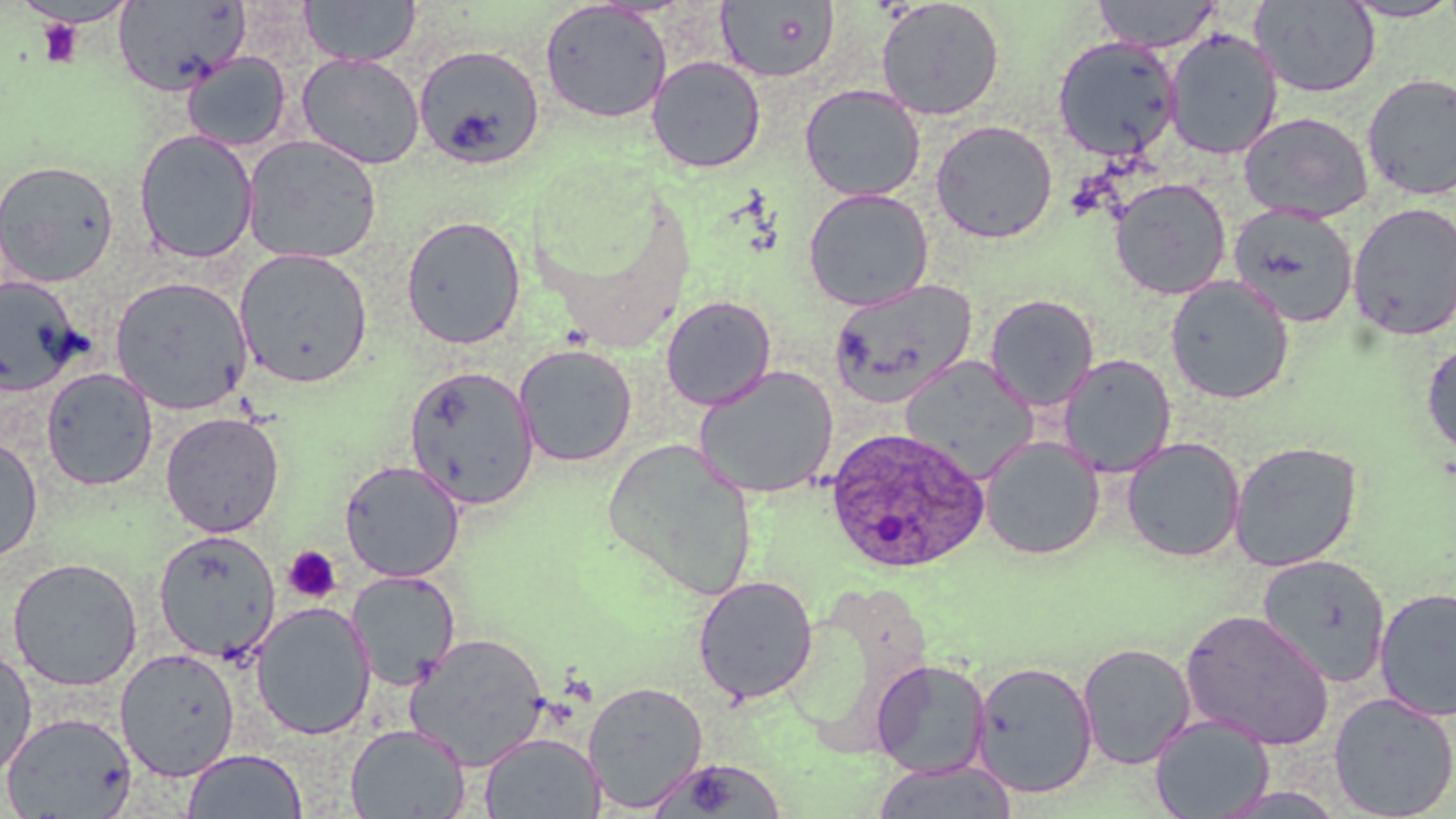

slide-level diagnosis = Plasmodium ovale
stain = May-Grünwald-Giemsa
uninfected red blood cell locations = approximate bounding boxes as (x1,y1)-(x2,y2) corner pairs in pixels: (299,0)-(421,66), (1092,0)-(1222,52), (1339,0)-(1456,22), (16,1)-(137,28), (113,1)-(249,95), (715,1)-(840,84), (875,1)-(1005,121), (1250,1)-(1381,98), (539,2)-(672,124), (1163,28)-(1283,160), (1052,36)-(1181,161), (414,44)-(546,169), (182,52)-(291,151), (296,53)-(426,169), (646,56)-(766,173), (1361,73)-(1456,201), (799,84)-(926,201), (1239,111)-(1373,223), (930,120)-(1058,243), (134,129)-(258,264), (241,134)-(383,265), (0,159)-(119,287), (1109,178)-(1232,300), (803,188)-(934,311), (1348,202)-(1456,342), (1228,203)-(1359,327), (401,215)-(526,349), (234,248)-(373,389), (1165,275)-(1295,404), (110,276)-(253,415), (0,277)-(85,396), (828,278)-(978,408), (984,294)-(1099,411), (660,295)-(777,411), (1421,339)-(1456,458), (514,344)-(638,468), (1058,354)-(1176,478), (901,356)-(1039,482), (405,365)-(540,508), (692,365)-(841,500), (41,368)-(158,491), (160,411)-(285,537), (0,435)-(43,565), (980,435)-(1104,560), (1121,437)-(1245,563), (603,440)-(759,601), (1229,440)-(1363,572), (339,460)-(465,582), (153,529)-(281,663), (1257,554)-(1390,688), (6,557)-(143,691), (347,570)-(461,692), (692,575)-(819,704), (1374,587)-(1456,722), (250,602)-(376,740), (1180,610)-(1334,750), (404,633)-(550,771), (1077,642)-(1196,769), (0,646)-(37,777), (115,647)-(240,782), (871,659)-(992,778), (971,660)-(1099,798), (583,680)-(709,813), (1328,692)-(1456,819), (1,711)-(137,819), (1149,714)-(1275,819), (345,723)-(470,818), (479,732)-(605,818), (182,748)-(307,819), (647,757)-(789,818), (872,760)-(1016,819)
field of view = one of a larger specimen
platelet locations = approximate bounding boxes as (x1,y1)-(x2,y2) corner pairs in pixels: (36,17)-(84,68), (283,545)-(342,603)
image size = 1456×819 pixels
Plasmodium ovale-infected red blood cell locations = approximate bounding boxes as (x1,y1)-(x2,y2) corner pairs in pixels: (824,426)-(989,575)
modality = optical microscopy
preparation = thin blood smear
magnification = 1000x